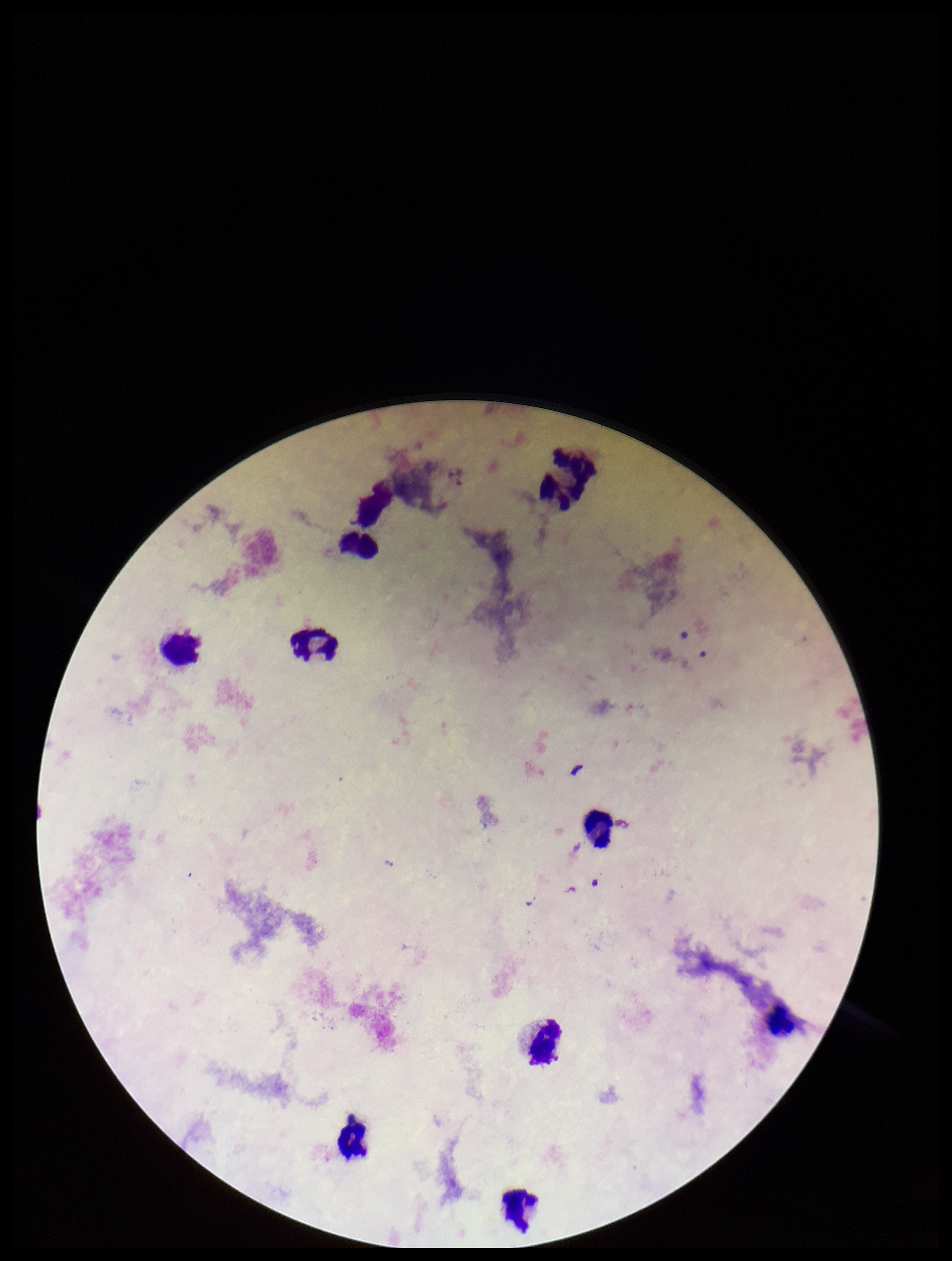

Summary:
  - Leukocyte count: 10
  - Field of view: one from this slide
  - Preparation: thick smear
  - Patient malaria status: negative
  - Plasmodium parasites: none identified
  - Capture: smartphone photograph through the microscope eyepiece
  - Image size: 952×1261 pixels
  - Parasite count: 0
  - Stain: Giemsa